Assess for malaria.
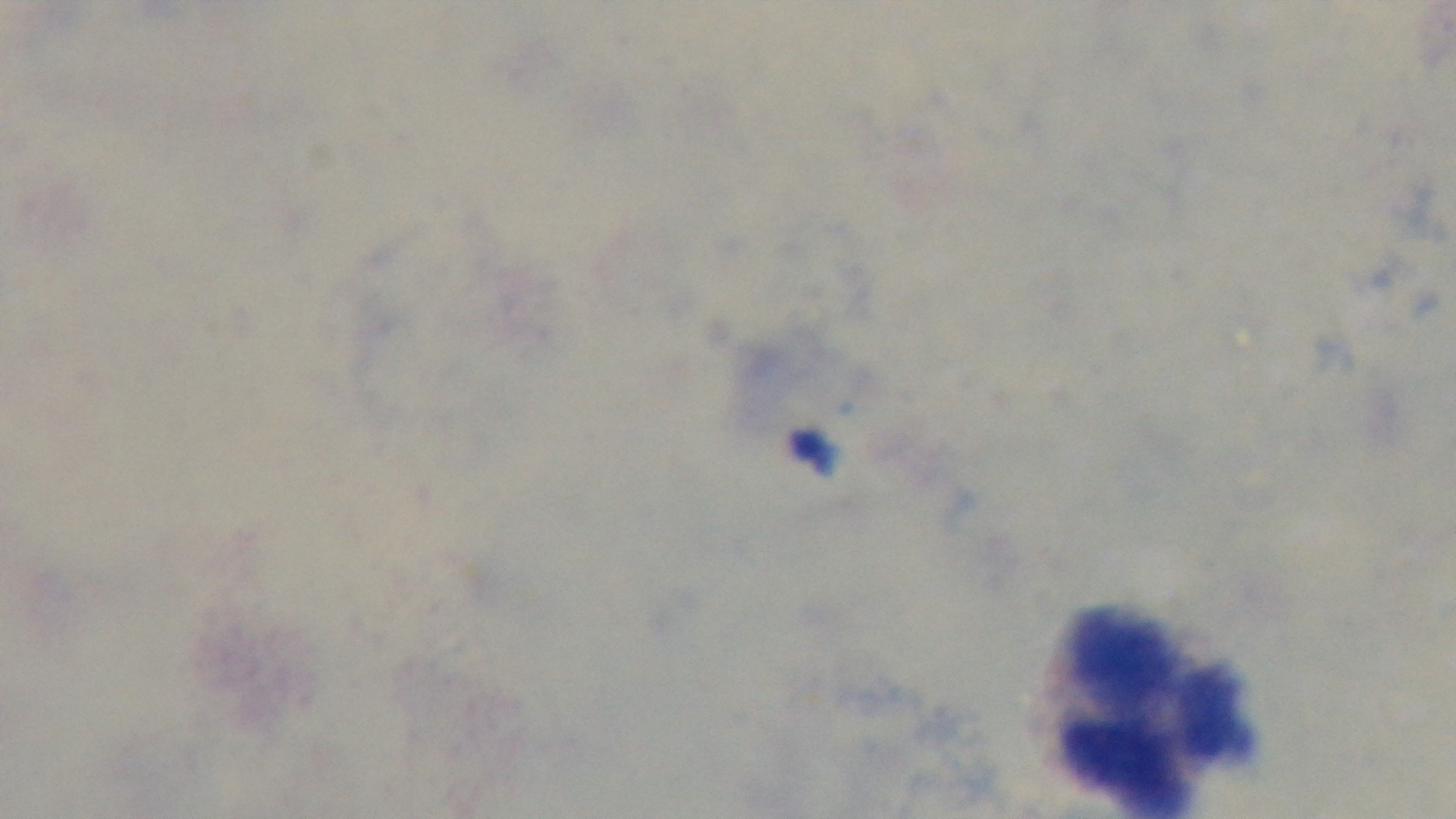

Negative.

Captured with a mounted 4K digital camera. Single field of view. 100x oil-immersion objective. Light microscopy. Giemsa stain. Preparation: thick smear.